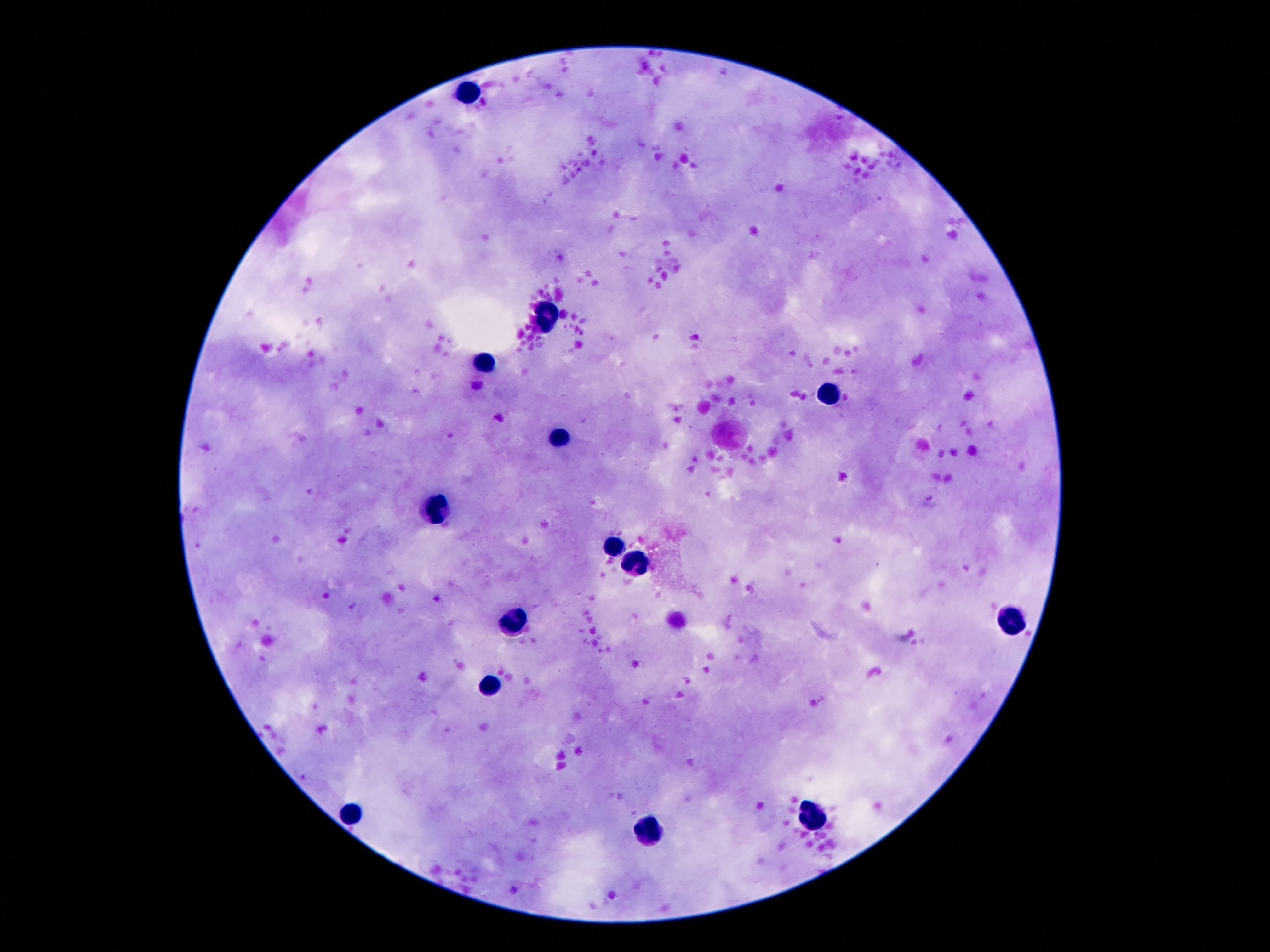
{
  "magnification": "100x",
  "leukocyte_locations": "approximate centers as [x, y] in pixels: [470, 89], [543, 319], [485, 359], [828, 393], [562, 438], [436, 511], [613, 544], [638, 566], [1014, 617], [514, 620], [492, 684], [812, 811], [350, 814], [653, 829]",
  "image_size": "1270×952 pixels",
  "preparation": "thick blood smear",
  "stain": "Giemsa",
  "capture": "smartphone camera through the microscope eyepiece",
  "field_of_view": "one from this slide",
  "patient_malaria_status": "negative"
}